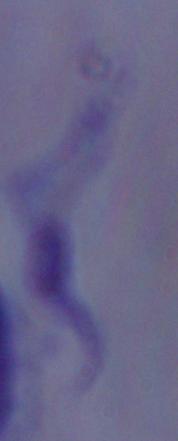

Micrograph. A trypanosome is seen. 1000x magnification.